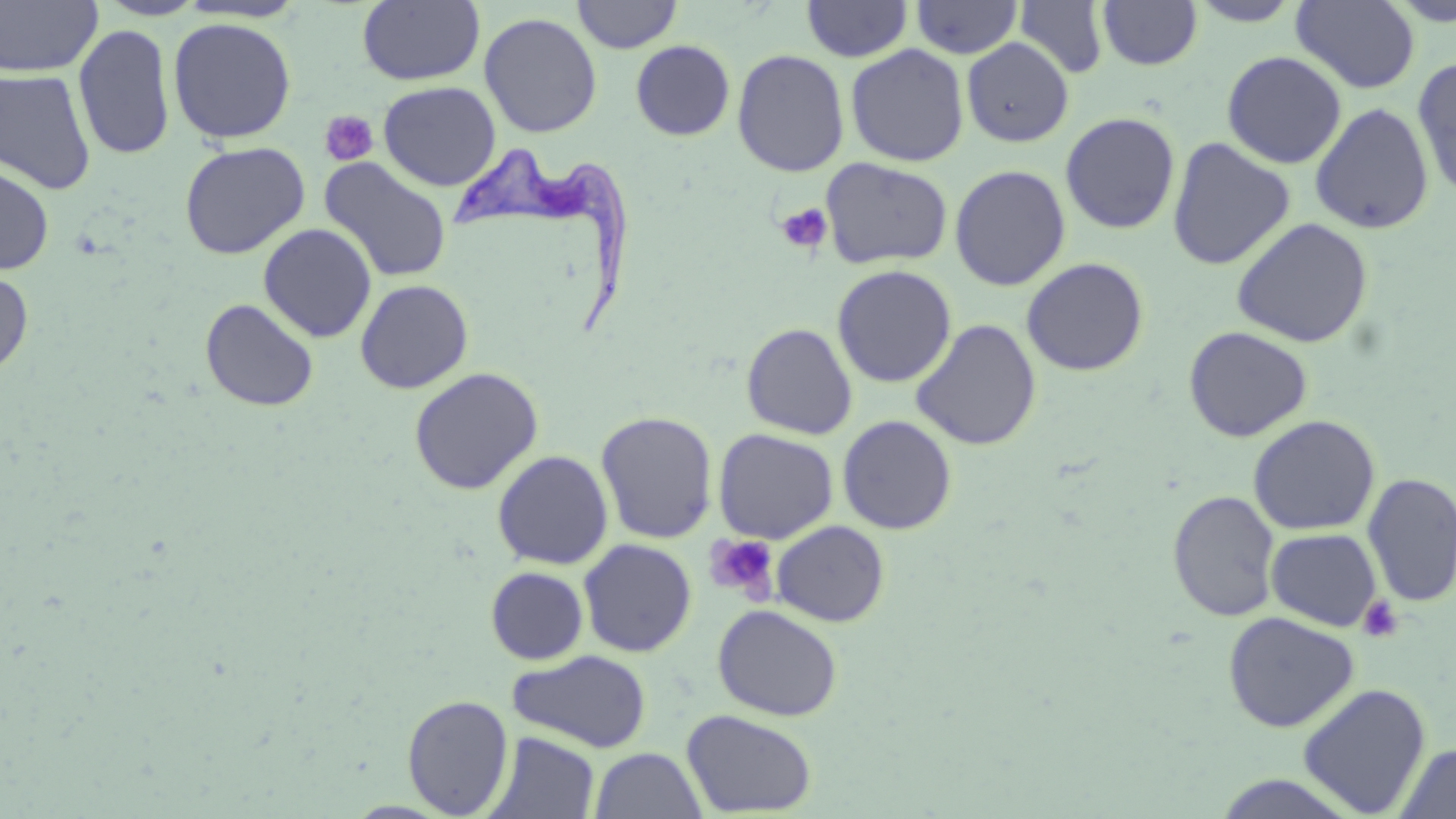

Approximate bounding boxes as named x1/y1/x2/y2 corners in pixels. Trypanosoma brucei locations: (x1=454, y1=137, x2=630, y2=335). Uninfected red blood cell locations: (x1=0, y1=0, x2=102, y2=78), (x1=95, y1=0, x2=209, y2=21), (x1=357, y1=0, x2=485, y2=86), (x1=572, y1=0, x2=682, y2=53), (x1=1014, y1=0, x2=1109, y2=79), (x1=176, y1=1, x2=308, y2=23), (x1=801, y1=1, x2=913, y2=62), (x1=911, y1=1, x2=1023, y2=59), (x1=1097, y1=1, x2=1202, y2=71), (x1=1187, y1=1, x2=1304, y2=27), (x1=1291, y1=1, x2=1420, y2=92), (x1=479, y1=12, x2=603, y2=139), (x1=168, y1=17, x2=296, y2=144), (x1=73, y1=24, x2=175, y2=160), (x1=961, y1=38, x2=1074, y2=147), (x1=630, y1=40, x2=735, y2=140), (x1=845, y1=44, x2=970, y2=167), (x1=732, y1=49, x2=850, y2=177), (x1=1221, y1=51, x2=1347, y2=169), (x1=1412, y1=58, x2=1456, y2=199), (x1=0, y1=69, x2=97, y2=194), (x1=378, y1=81, x2=501, y2=191), (x1=1310, y1=102, x2=1434, y2=235), (x1=1060, y1=112, x2=1180, y2=234), (x1=1167, y1=137, x2=1296, y2=271), (x1=179, y1=141, x2=310, y2=259), (x1=318, y1=157, x2=453, y2=283), (x1=820, y1=157, x2=953, y2=270), (x1=0, y1=164, x2=54, y2=275), (x1=949, y1=164, x2=1071, y2=291), (x1=1232, y1=217, x2=1373, y2=348), (x1=258, y1=223, x2=377, y2=343), (x1=1021, y1=257, x2=1149, y2=377), (x1=831, y1=264, x2=957, y2=388), (x1=0, y1=268, x2=34, y2=378), (x1=355, y1=279, x2=474, y2=394), (x1=200, y1=298, x2=319, y2=412), (x1=911, y1=318, x2=1042, y2=451), (x1=741, y1=322, x2=858, y2=439), (x1=1183, y1=325, x2=1313, y2=443), (x1=409, y1=366, x2=544, y2=495), (x1=595, y1=411, x2=719, y2=544), (x1=837, y1=415, x2=957, y2=535), (x1=1248, y1=415, x2=1381, y2=535), (x1=713, y1=428, x2=839, y2=543), (x1=492, y1=450, x2=613, y2=570), (x1=1362, y1=471, x2=1456, y2=608), (x1=1168, y1=490, x2=1281, y2=622), (x1=772, y1=520, x2=890, y2=627), (x1=1266, y1=527, x2=1381, y2=631), (x1=578, y1=538, x2=698, y2=658), (x1=485, y1=566, x2=588, y2=665), (x1=712, y1=604, x2=843, y2=722), (x1=1222, y1=611, x2=1360, y2=732), (x1=508, y1=649, x2=652, y2=753), (x1=1297, y1=682, x2=1432, y2=817), (x1=402, y1=694, x2=515, y2=817), (x1=681, y1=709, x2=818, y2=817), (x1=486, y1=731, x2=600, y2=818), (x1=1394, y1=742, x2=1456, y2=819), (x1=589, y1=747, x2=707, y2=819), (x1=1209, y1=772, x2=1360, y2=817). Platelet locations: (x1=319, y1=110, x2=379, y2=167), (x1=775, y1=202, x2=833, y2=255), (x1=704, y1=534, x2=780, y2=600), (x1=1358, y1=595, x2=1405, y2=643). Slide-level diagnosis: Trypanosoma brucei. One field of a larger specimen. Captured at 1000x magnification. Optical microscopy. Thin blood film. Image is 1456×819 pixels. May-Grünwald-Giemsa stain.